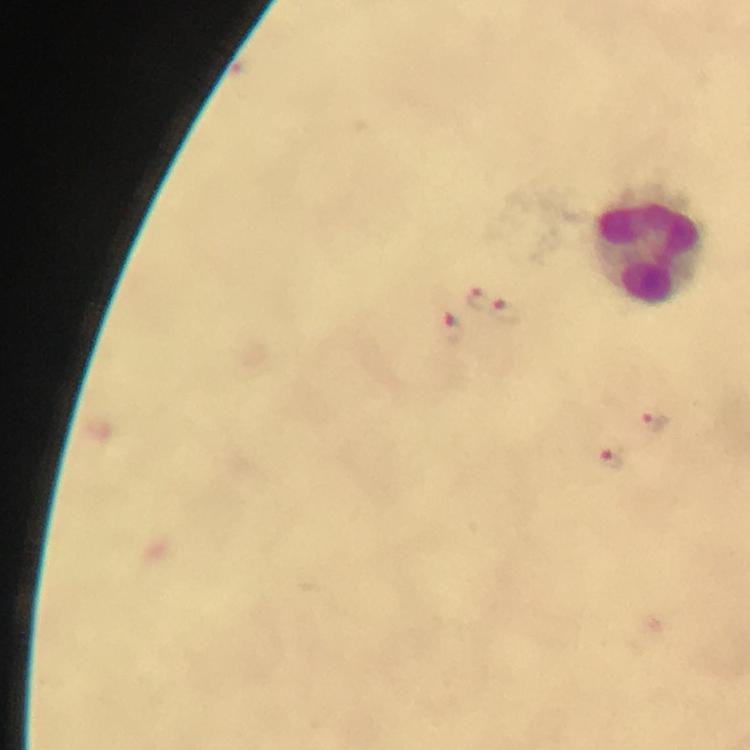
Approximate centers as {x, y} in pixels.
Summary:
  - Leukocyte locations: {651, 247}
  - Plasmodium parasite locations: {477, 301}, {506, 313}, {452, 328}, {654, 421}, {611, 458}
  - Capture: smartphone photograph through a microscope
  - Immersion oil: used
  - Preparation: thick smear
  - Context: from a diagnostic examination for malaria
  - Image size: 750×750 pixels
  - Cropped from: one field of view
  - Stain: Giemsa
  - Magnification: 100x